Classify this cell by malaria status.
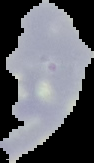

It is uninfected.

From a thin blood film. The area outside the segmented cell region is set to black. Image is 94×163 pixels.